State the blood parasite species.
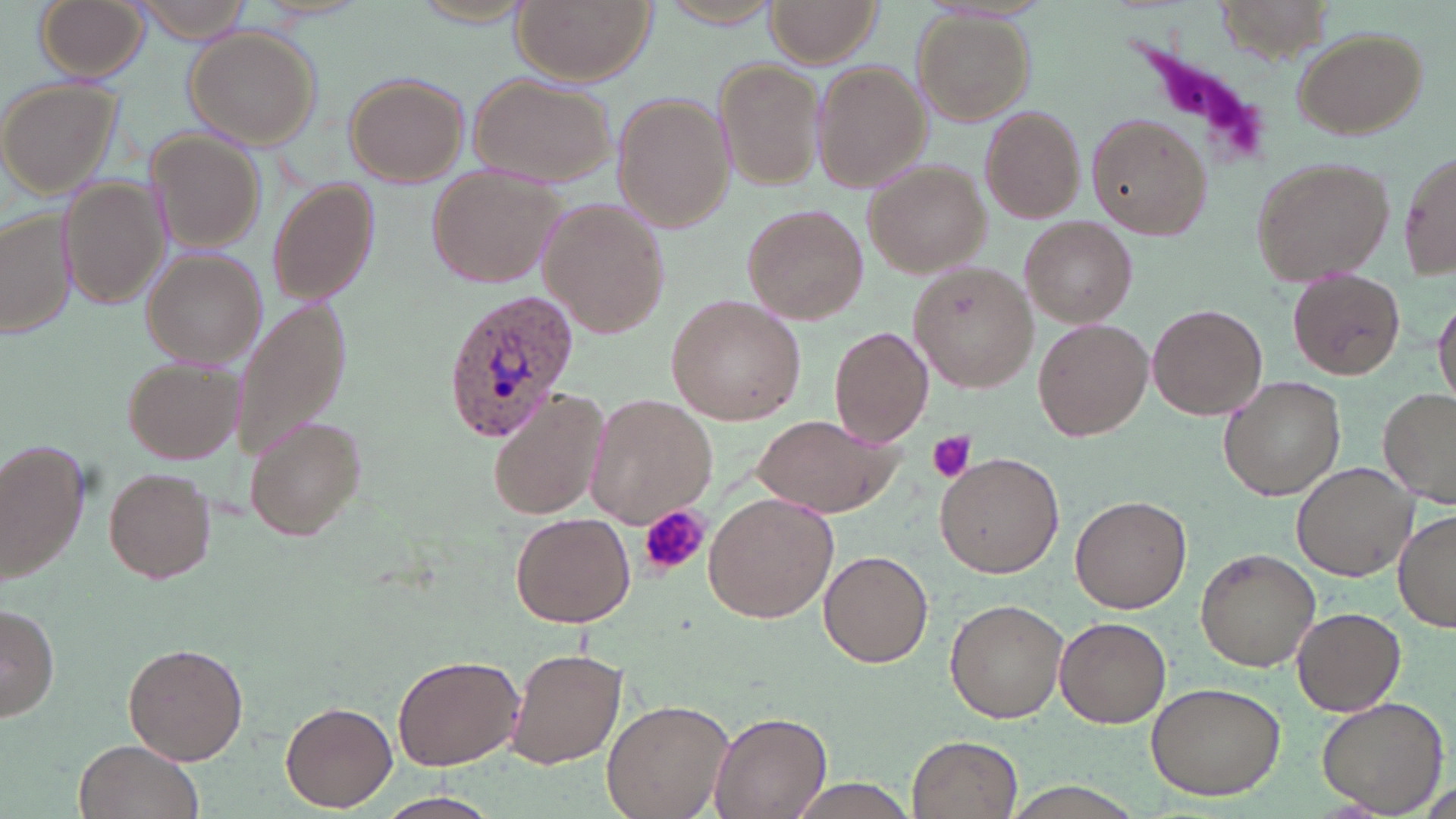

Plasmodium ovale.

preparation = thin blood film
uninfected red blood cell locations = approximate bounding boxes as [x1, y1, x2, y2] in pixels: [33, 0, 151, 82], [402, 0, 540, 29], [511, 0, 657, 86], [133, 1, 256, 42], [655, 1, 784, 28], [767, 1, 880, 67], [912, 14, 1032, 125], [184, 26, 322, 149], [1291, 28, 1427, 140], [717, 59, 822, 190], [811, 60, 931, 193], [343, 71, 469, 187], [468, 73, 614, 187], [1, 78, 124, 200], [612, 95, 734, 231], [979, 106, 1085, 223], [1087, 112, 1214, 240], [144, 130, 261, 251], [1398, 146, 1454, 283], [1249, 154, 1394, 286], [862, 160, 992, 278], [426, 168, 565, 289], [60, 176, 171, 312], [267, 180, 378, 305], [537, 199, 670, 336], [741, 204, 871, 325], [0, 206, 77, 342], [1021, 215, 1136, 327], [143, 250, 266, 367], [908, 261, 1040, 391], [1288, 269, 1405, 381], [1432, 291, 1456, 412], [669, 294, 808, 425], [233, 300, 352, 460], [1148, 304, 1268, 422], [1033, 318, 1154, 441], [829, 325, 934, 444], [123, 357, 241, 464], [1217, 376, 1347, 501], [1379, 386, 1456, 505], [488, 388, 609, 520], [583, 395, 716, 526], [751, 413, 906, 517], [242, 416, 367, 541], [0, 443, 85, 579], [935, 452, 1063, 577], [1291, 461, 1423, 582], [105, 469, 215, 583], [704, 491, 839, 623], [1070, 496, 1191, 615], [1393, 507, 1455, 632], [511, 511, 637, 627], [1196, 549, 1318, 672], [819, 550, 934, 668], [945, 596, 1069, 723], [1, 605, 58, 722], [1292, 606, 1405, 715], [1055, 615, 1172, 728], [123, 642, 248, 765], [506, 647, 628, 770], [393, 654, 525, 771], [1144, 681, 1286, 801], [1316, 696, 1449, 815], [602, 698, 733, 819], [282, 701, 398, 810], [708, 711, 831, 819], [907, 735, 1021, 818], [74, 737, 205, 819], [786, 776, 923, 819], [1000, 784, 1145, 817], [373, 791, 502, 819]
modality = light microscopy
platelet locations = approximate bounding boxes as [x1, y1, x2, y2] in pixels: [1113, 29, 1279, 171], [926, 431, 975, 483], [637, 506, 710, 573]
magnification = 1000x
stain = May-Grünwald-Giemsa
field of view = single
Plasmodium ovale-infected red blood cell locations = approximate bounding boxes as [x1, y1, x2, y2] in pixels: [443, 288, 581, 441]
image size = 1456×819 pixels